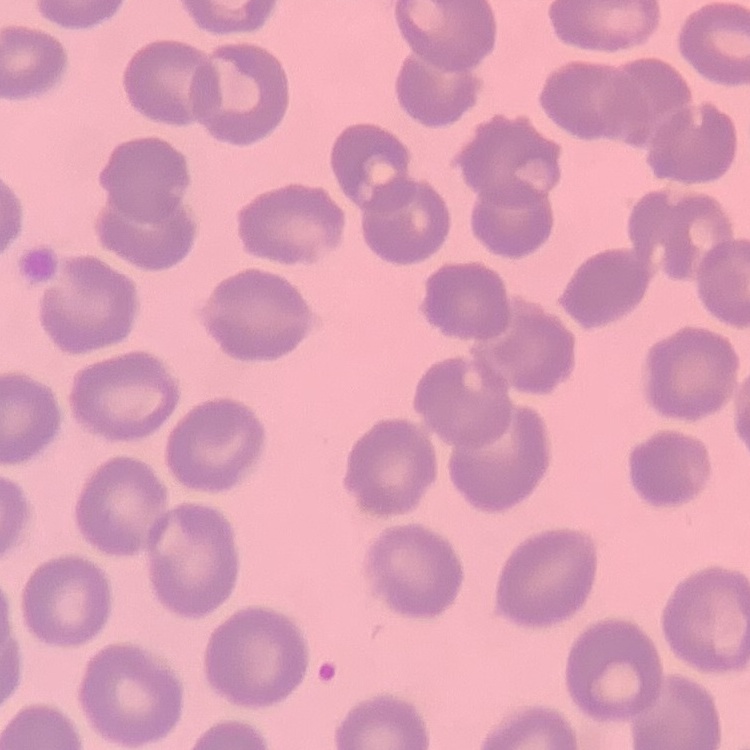

The erythrocytes show no rouleaux formation. One tile cut from a larger photomicrograph. Field's or Giemsa stain. Thin peripheral smear.